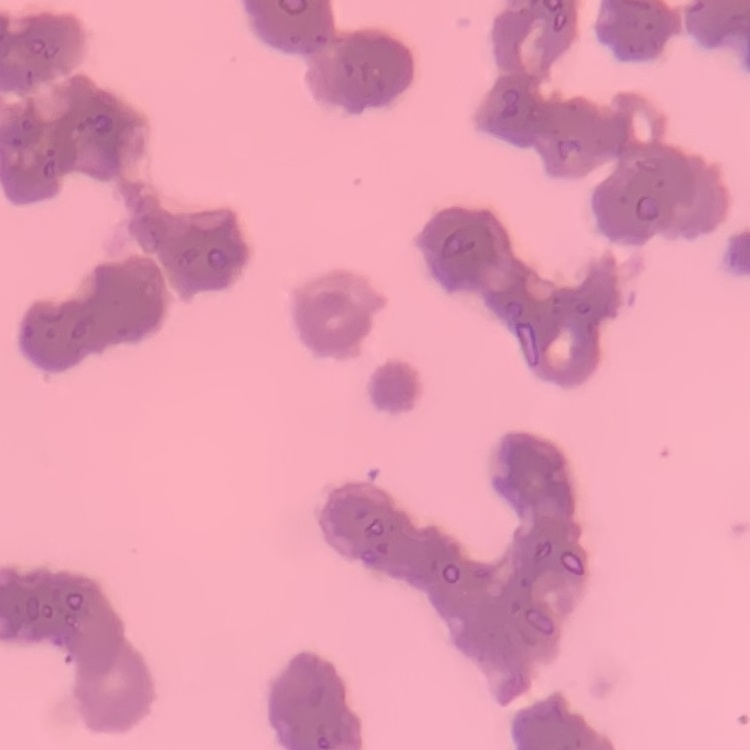
Summary:
  - Red blood cell morphology: rouleaux formation
  - Preparation: thin blood smear
  - Image type: square crop of a larger photomicrograph
  - Stain: Field's or Giemsa